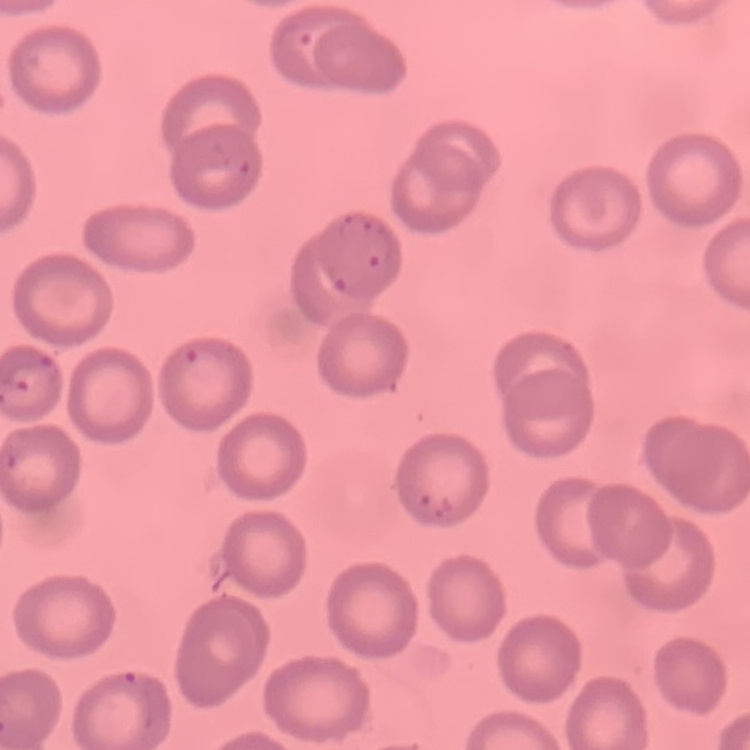

erythrocyte morphology = no rouleaux formation
preparation = thin peripheral smear
image type = one tile cut from a larger photomicrograph
stain = Field's or Giemsa